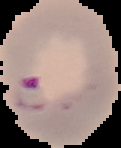

Summary:
  - Preparation: thin blood film
  - Result: Plasmodium parasites identified
  - Image type: cell region segmented out of the field of view; surrounding area masked to black
  - Image size: 121×148 pixels